State which parasite is depicted.
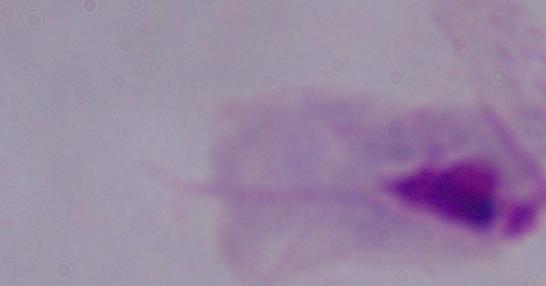
This is a trichomonad.

{
  "modality": "micrograph",
  "magnification": "1000x"
}